Point out each malaria parasite.
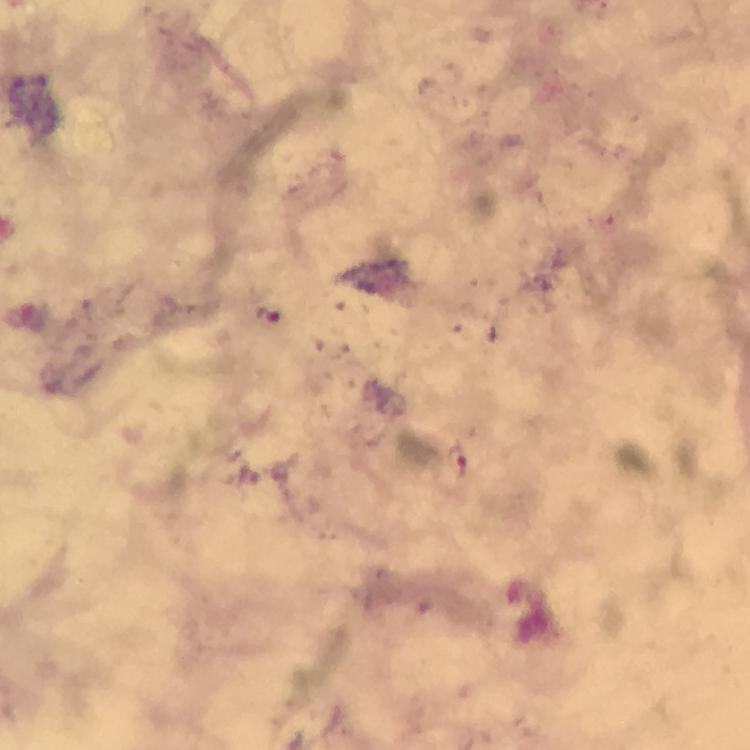
Approximate centers as (x, y) in pixels.
Malaria parasites: (269, 313), (453, 462).

Summary:
  - Immersion oil: used
  - Magnification: 100x
  - Stain: Giemsa
  - Cropped from: one field of view
  - Preparation: thick blood smear
  - Capture: smartphone camera through the microscope
  - Context: from a malaria diagnostic workup
  - Image size: 750×750 pixels